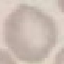 Malaria status: uninfected. Thin blood smear. Automatically extracted cell patch, resized to 64 × 64 pixels. Giemsa stain. Acquired by smartphone through the microscope eyepiece.